Assess this cell for malaria.
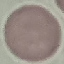
It is uninfected.

preparation = thin smear
stain = Giemsa
image type = cell patch, automatically extracted from a larger field of view and resized to 64 × 64 pixels
capture = smartphone camera at the microscope eyepiece